Give the extent of all Plasmodium vivax-infected red blood cells.
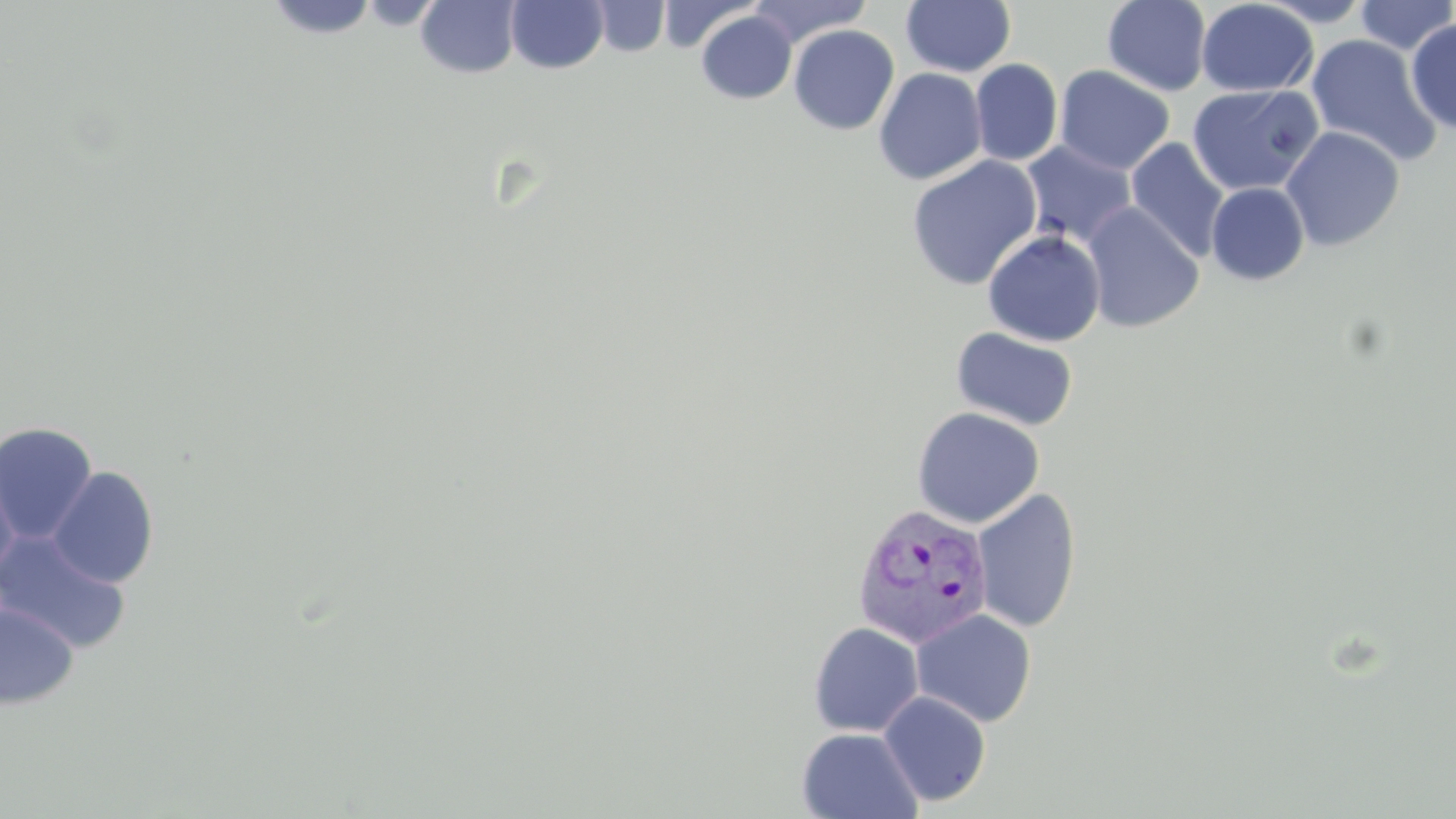

Approximate bounding boxes as named x1/y1/x2/y2 corners in pixels.
Plasmodium vivax-infected red blood cells: (x1=851, y1=503, x2=994, y2=650).

slide_level_diagnosis: Plasmodium vivax
stain: May-Grünwald-Giemsa
preparation: thin blood smear
uninfected_red_blood_cell_locations: 'approximate bounding boxes as named x1/y1/x2/y2 corners in pixels: (x1=505, y1=0, x2=608, y2=73), (x1=590, y1=0, x2=670, y2=58), (x1=749, y1=0, x2=872, y2=48), (x1=1102, y1=0, x2=1212, y2=95), (x1=1196, y1=0, x2=1318, y2=97), (x1=1255, y1=0, x2=1376, y2=26), (x1=1355, y1=0, x2=1456, y2=55), (x1=271, y1=1, x2=378, y2=42), (x1=416, y1=1, x2=521, y2=79), (x1=657, y1=1, x2=760, y2=54), (x1=902, y1=1, x2=1016, y2=77), (x1=697, y1=10, x2=796, y2=104), (x1=1406, y1=18, x2=1456, y2=134), (x1=788, y1=25, x2=899, y2=135), (x1=1305, y1=33, x2=1441, y2=166), (x1=970, y1=59, x2=1063, y2=167), (x1=1055, y1=65, x2=1175, y2=175), (x1=873, y1=67, x2=987, y2=185), (x1=1187, y1=84, x2=1323, y2=195), (x1=1281, y1=126, x2=1405, y2=251), (x1=1125, y1=138, x2=1229, y2=261), (x1=1021, y1=140, x2=1137, y2=248), (x1=906, y1=155, x2=1043, y2=291), (x1=1206, y1=182, x2=1310, y2=285), (x1=1081, y1=202, x2=1204, y2=333), (x1=983, y1=230, x2=1105, y2=347), (x1=951, y1=326, x2=1079, y2=432), (x1=911, y1=406, x2=1045, y2=528), (x1=0, y1=422, x2=98, y2=543), (x1=0, y1=461, x2=20, y2=585), (x1=47, y1=466, x2=159, y2=588), (x1=971, y1=488, x2=1082, y2=633), (x1=0, y1=530, x2=131, y2=653), (x1=0, y1=602, x2=78, y2=709), (x1=911, y1=608, x2=1037, y2=727), (x1=808, y1=621, x2=924, y2=737), (x1=878, y1=690, x2=991, y2=808), (x1=797, y1=727, x2=923, y2=818)'
magnification: 1000x
image_size: 1456×819 pixels
field_of_view: one of a larger specimen
modality: optical microscopy